Assess this cell for malaria.
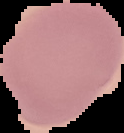
It is uninfected.

image type = cell region segmented out of the field of view; surrounding area masked to black
preparation = thin blood film
image size = 124×133 pixels